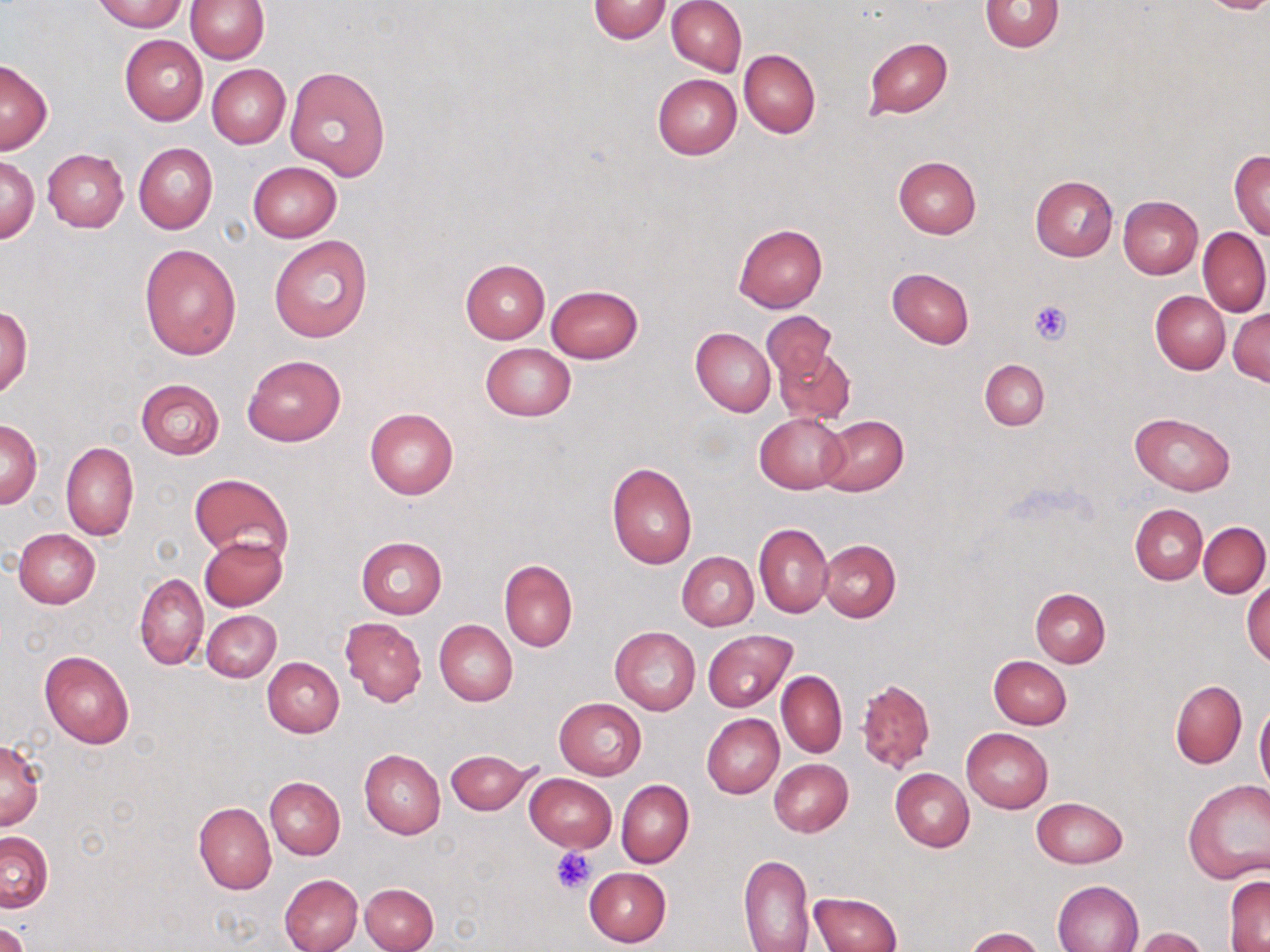
Summary:
  - Coordinate format: approximate bounding boxes as named x1/y1/x2/y2 corners in pixels
  - Uninfected red blood cell locations: (x1=93, y1=0, x2=186, y2=32), (x1=186, y1=0, x2=268, y2=63), (x1=588, y1=0, x2=671, y2=43), (x1=667, y1=0, x2=747, y2=76), (x1=979, y1=1, x2=1066, y2=52), (x1=119, y1=35, x2=208, y2=125), (x1=862, y1=37, x2=954, y2=120), (x1=739, y1=50, x2=821, y2=137), (x1=1, y1=60, x2=52, y2=153), (x1=207, y1=64, x2=290, y2=148), (x1=285, y1=65, x2=391, y2=182), (x1=652, y1=74, x2=742, y2=159), (x1=133, y1=142, x2=218, y2=234), (x1=42, y1=148, x2=128, y2=231), (x1=1229, y1=149, x2=1270, y2=239), (x1=1, y1=156, x2=39, y2=243), (x1=894, y1=156, x2=981, y2=239), (x1=248, y1=161, x2=342, y2=242), (x1=1030, y1=175, x2=1119, y2=261), (x1=1118, y1=196, x2=1204, y2=279), (x1=734, y1=222, x2=827, y2=312), (x1=1198, y1=228, x2=1270, y2=316), (x1=268, y1=235, x2=372, y2=343), (x1=139, y1=244, x2=242, y2=359), (x1=461, y1=259, x2=549, y2=343), (x1=887, y1=267, x2=974, y2=348), (x1=545, y1=284, x2=643, y2=364), (x1=1151, y1=290, x2=1230, y2=374), (x1=0, y1=307, x2=32, y2=398), (x1=1228, y1=307, x2=1270, y2=386), (x1=761, y1=311, x2=836, y2=386), (x1=691, y1=327, x2=776, y2=416), (x1=480, y1=342, x2=575, y2=421), (x1=774, y1=346, x2=855, y2=425), (x1=243, y1=355, x2=345, y2=446), (x1=980, y1=359, x2=1048, y2=431), (x1=135, y1=379, x2=224, y2=459), (x1=365, y1=407, x2=459, y2=500), (x1=1129, y1=411, x2=1236, y2=495), (x1=755, y1=413, x2=848, y2=493), (x1=818, y1=415, x2=908, y2=496), (x1=1, y1=420, x2=43, y2=508), (x1=61, y1=442, x2=139, y2=542), (x1=606, y1=461, x2=697, y2=569), (x1=189, y1=472, x2=292, y2=562), (x1=1130, y1=504, x2=1208, y2=584), (x1=1199, y1=522, x2=1269, y2=596), (x1=755, y1=523, x2=834, y2=616), (x1=14, y1=528, x2=101, y2=608), (x1=199, y1=534, x2=287, y2=611), (x1=356, y1=537, x2=446, y2=619), (x1=818, y1=540, x2=901, y2=623), (x1=677, y1=552, x2=758, y2=630), (x1=498, y1=559, x2=577, y2=652), (x1=135, y1=574, x2=209, y2=670), (x1=1243, y1=579, x2=1270, y2=666), (x1=1030, y1=588, x2=1111, y2=667), (x1=202, y1=610, x2=281, y2=682), (x1=340, y1=617, x2=427, y2=706), (x1=434, y1=620, x2=517, y2=706), (x1=610, y1=626, x2=701, y2=715), (x1=703, y1=630, x2=796, y2=711), (x1=40, y1=650, x2=135, y2=750), (x1=988, y1=656, x2=1071, y2=730), (x1=263, y1=657, x2=345, y2=737), (x1=776, y1=671, x2=846, y2=758), (x1=856, y1=679, x2=935, y2=775), (x1=1170, y1=680, x2=1247, y2=767), (x1=554, y1=698, x2=646, y2=779), (x1=1254, y1=701, x2=1270, y2=792), (x1=701, y1=714, x2=783, y2=798), (x1=961, y1=726, x2=1053, y2=813), (x1=0, y1=739, x2=45, y2=832), (x1=445, y1=748, x2=538, y2=814), (x1=358, y1=749, x2=445, y2=839), (x1=769, y1=759, x2=854, y2=836), (x1=891, y1=769, x2=974, y2=852), (x1=524, y1=774, x2=617, y2=852), (x1=266, y1=777, x2=345, y2=859), (x1=616, y1=779, x2=694, y2=867), (x1=1183, y1=780, x2=1270, y2=883), (x1=1032, y1=797, x2=1127, y2=867), (x1=193, y1=802, x2=275, y2=894), (x1=0, y1=831, x2=53, y2=912), (x1=737, y1=853, x2=815, y2=952), (x1=583, y1=867, x2=672, y2=946), (x1=279, y1=873, x2=363, y2=952), (x1=1225, y1=876, x2=1270, y2=950), (x1=1053, y1=880, x2=1144, y2=952), (x1=361, y1=882, x2=439, y2=952), (x1=809, y1=891, x2=902, y2=952), (x1=0, y1=922, x2=28, y2=952), (x1=965, y1=927, x2=1044, y2=952), (x1=1132, y1=927, x2=1209, y2=952)
  - Platelet locations: (x1=1029, y1=299, x2=1073, y2=344), (x1=550, y1=848, x2=595, y2=895)
  - Slide-level diagnosis: no evidence of blood parasites
  - Magnification: 1000x
  - Stain: May-Grünwald-Giemsa
  - Modality: light microscopy
  - Image size: 1270×952 pixels
  - Preparation: thin blood smear
  - Field of view: single